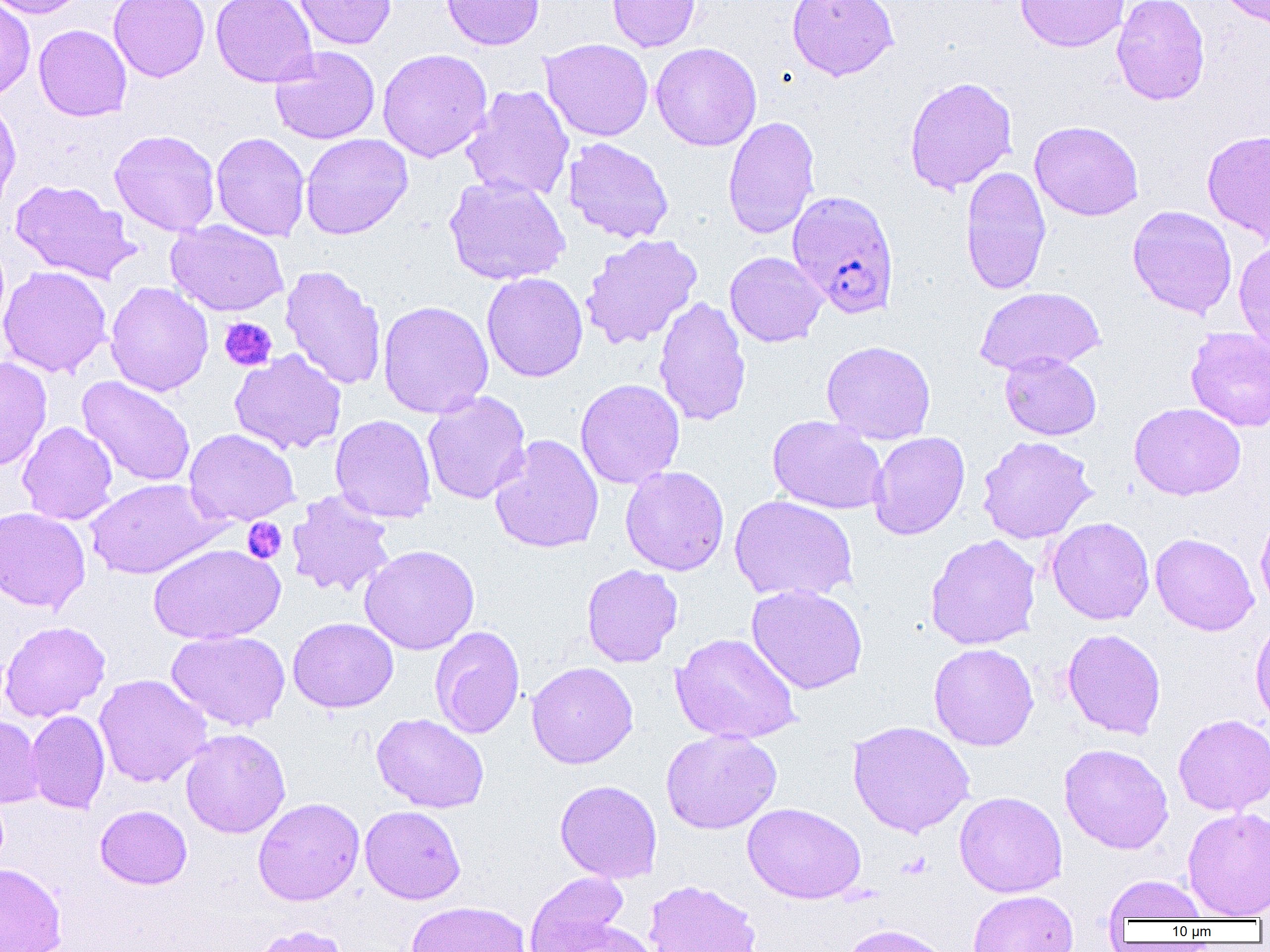
Summary:
  - Coordinate format: approximate bounding boxes as [x1, y1, x2, y2] in pixels
  - Uninfected red blood cell locations: [0, 0, 89, 19], [108, 0, 210, 82], [211, 0, 318, 88], [293, 0, 397, 50], [441, 0, 544, 50], [607, 0, 701, 52], [786, 0, 899, 81], [1016, 0, 1129, 53], [1111, 0, 1209, 106], [1214, 0, 1269, 31], [0, 1, 36, 102], [34, 24, 132, 121], [540, 38, 653, 142], [651, 42, 762, 151], [269, 46, 380, 144], [377, 48, 493, 162], [904, 76, 1018, 194], [461, 84, 574, 202], [0, 95, 22, 214], [722, 115, 820, 239], [1029, 120, 1144, 221], [109, 129, 221, 236], [1201, 130, 1270, 245], [211, 132, 310, 241], [300, 133, 413, 240], [563, 137, 675, 243], [960, 166, 1052, 295], [444, 175, 570, 286], [10, 179, 139, 285], [1127, 205, 1237, 318], [166, 220, 289, 316], [579, 233, 702, 350], [1234, 239, 1270, 355], [724, 252, 827, 347], [0, 265, 112, 378], [281, 265, 387, 392], [481, 273, 588, 382], [105, 281, 214, 396], [974, 286, 1106, 375], [653, 295, 751, 427], [378, 300, 493, 419], [1185, 327, 1270, 431], [821, 340, 936, 445], [229, 349, 347, 455], [1000, 352, 1102, 440], [0, 356, 52, 471], [76, 375, 196, 488], [575, 378, 685, 489], [422, 391, 531, 504], [1129, 402, 1246, 500], [330, 414, 437, 524], [767, 415, 888, 515], [18, 421, 118, 525], [184, 428, 299, 526], [868, 432, 970, 540], [489, 434, 604, 554], [977, 435, 1098, 544], [620, 465, 729, 576], [85, 478, 223, 579], [287, 490, 396, 599], [729, 495, 858, 602], [1255, 504, 1270, 615], [0, 506, 91, 614], [1046, 517, 1155, 625], [925, 533, 1041, 650], [1150, 533, 1259, 636], [147, 542, 285, 645], [360, 544, 479, 655], [581, 564, 683, 668], [746, 583, 868, 694], [1250, 614, 1270, 730], [288, 617, 398, 713], [0, 620, 110, 723], [430, 625, 525, 739], [1062, 628, 1166, 739], [166, 630, 291, 731], [670, 633, 802, 744], [928, 643, 1039, 751], [526, 661, 638, 769], [94, 674, 211, 788], [26, 710, 110, 815], [371, 712, 489, 813], [1173, 713, 1270, 816], [0, 714, 44, 808], [847, 720, 975, 837], [180, 728, 291, 838], [661, 729, 782, 834], [1059, 743, 1174, 854], [554, 779, 662, 883], [954, 791, 1067, 898], [252, 796, 365, 906], [743, 802, 866, 904], [95, 805, 192, 889], [360, 805, 466, 904], [1182, 806, 1270, 919], [0, 863, 66, 952], [523, 871, 629, 951], [1103, 875, 1208, 923], [643, 880, 762, 952], [967, 889, 1078, 952], [406, 900, 532, 952], [547, 921, 658, 952], [839, 923, 953, 952], [252, 924, 349, 952]
  - Platelet locations: [219, 317, 277, 372], [242, 517, 287, 564]
  - Plasmodium falciparum-infected red blood cell locations: [787, 190, 899, 319]
  - Slide-level diagnosis: Plasmodium falciparum
  - Magnification: 1000x
  - Field of view: single
  - Modality: light microscopy
  - Preparation: thin blood film
  - Image size: 1270×952 pixels